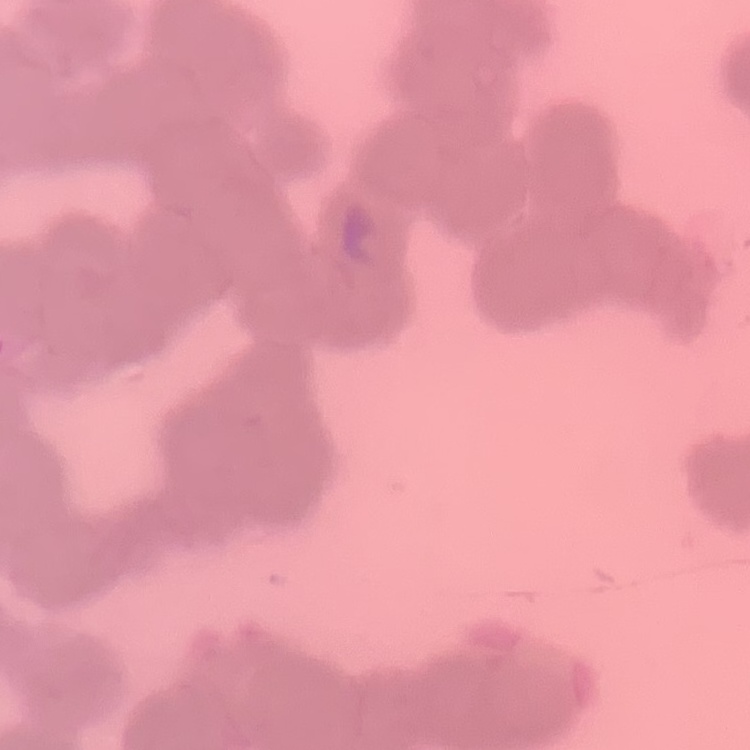 The red blood cells show rouleaux formation. Thin blood film. Stained with either Field's or Giemsa. One tile cut from a larger photomicrograph.